Report the malaria status of this cell.
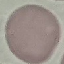
It is uninfected.

preparation = thin blood smear
stain = Giemsa
capture = smartphone camera at the microscope eyepiece
image type = cell patch, automatically extracted from a larger field of view and resized to 64 × 64 pixels